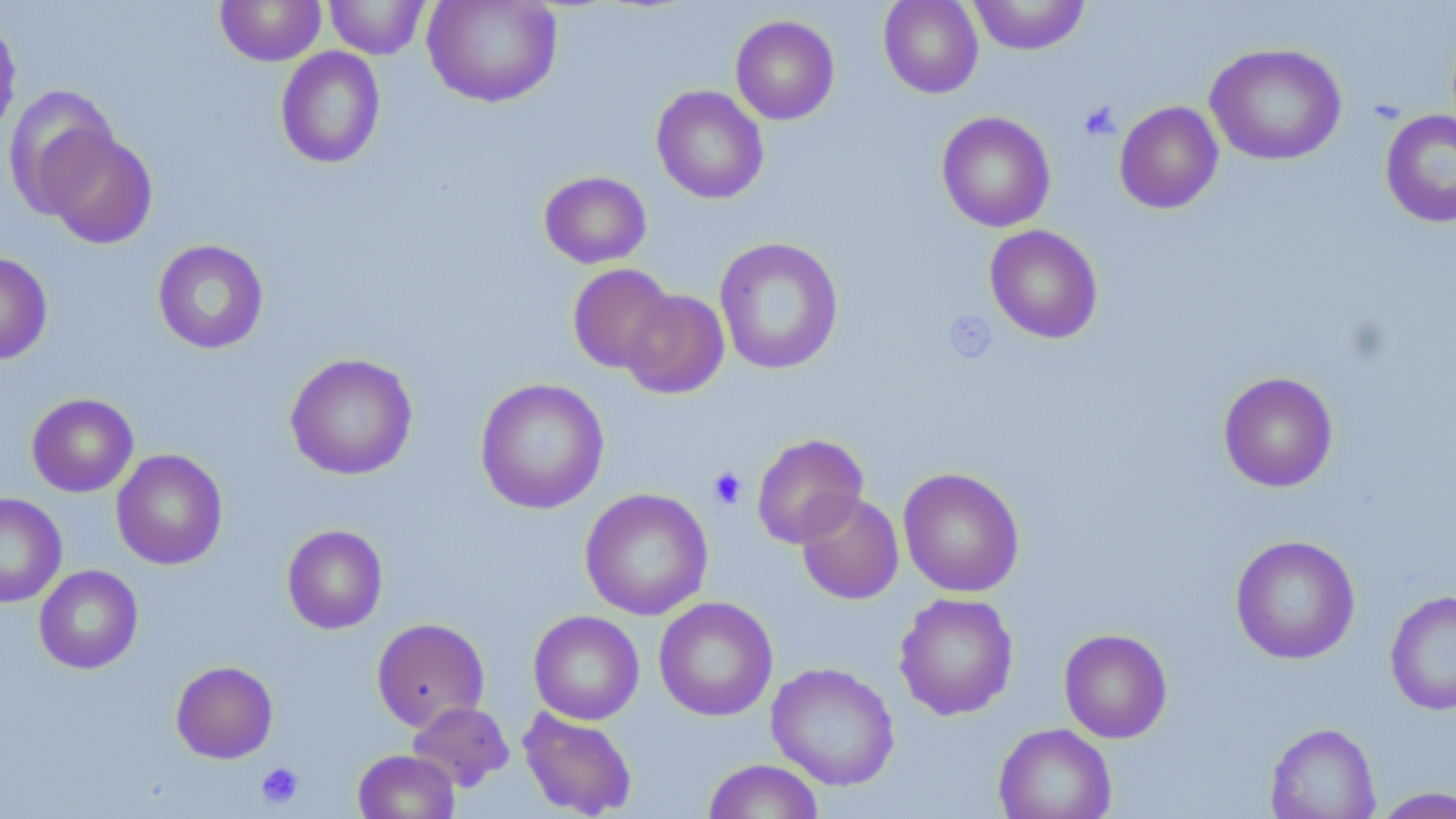
Summary:
  - Coordinate format: approximate bounding boxes as named x1/y1/x2/y2 corners in pixels
  - Uninfected red blood cell locations: (x1=215, y1=0, x2=326, y2=66), (x1=324, y1=0, x2=430, y2=59), (x1=422, y1=0, x2=563, y2=108), (x1=879, y1=0, x2=984, y2=98), (x1=968, y1=0, x2=1090, y2=55), (x1=0, y1=11, x2=22, y2=141), (x1=730, y1=15, x2=840, y2=125), (x1=1205, y1=42, x2=1347, y2=166), (x1=275, y1=46, x2=386, y2=169), (x1=4, y1=84, x2=120, y2=217), (x1=651, y1=85, x2=769, y2=204), (x1=1114, y1=101, x2=1224, y2=214), (x1=1379, y1=109, x2=1456, y2=228), (x1=936, y1=111, x2=1056, y2=233), (x1=43, y1=129, x2=158, y2=249), (x1=538, y1=171, x2=652, y2=269), (x1=984, y1=225, x2=1104, y2=344), (x1=714, y1=237, x2=844, y2=375), (x1=152, y1=239, x2=269, y2=354), (x1=0, y1=252, x2=53, y2=365), (x1=567, y1=263, x2=676, y2=374), (x1=620, y1=289, x2=730, y2=400), (x1=285, y1=353, x2=418, y2=480), (x1=1218, y1=371, x2=1338, y2=492), (x1=475, y1=378, x2=610, y2=514), (x1=26, y1=393, x2=139, y2=497), (x1=751, y1=433, x2=869, y2=548), (x1=111, y1=449, x2=228, y2=570), (x1=898, y1=467, x2=1025, y2=598), (x1=579, y1=487, x2=713, y2=621), (x1=795, y1=491, x2=904, y2=605), (x1=0, y1=493, x2=67, y2=608), (x1=282, y1=524, x2=388, y2=634), (x1=1230, y1=534, x2=1360, y2=664), (x1=33, y1=565, x2=143, y2=674), (x1=1385, y1=589, x2=1456, y2=716), (x1=894, y1=592, x2=1019, y2=720), (x1=654, y1=596, x2=778, y2=722), (x1=528, y1=610, x2=644, y2=725), (x1=371, y1=617, x2=490, y2=732), (x1=1059, y1=628, x2=1172, y2=743), (x1=170, y1=660, x2=278, y2=763), (x1=766, y1=662, x2=900, y2=791), (x1=407, y1=701, x2=514, y2=792), (x1=517, y1=707, x2=638, y2=819), (x1=1265, y1=722, x2=1380, y2=819), (x1=993, y1=723, x2=1117, y2=819), (x1=353, y1=749, x2=459, y2=819), (x1=702, y1=759, x2=825, y2=819), (x1=1370, y1=787, x2=1456, y2=818)
  - Platelet locations: (x1=1079, y1=101, x2=1121, y2=142), (x1=943, y1=310, x2=998, y2=364), (x1=708, y1=466, x2=747, y2=509), (x1=256, y1=762, x2=305, y2=809)
  - Slide-level diagnosis: no evidence of blood parasites
  - Preparation: thin blood smear
  - Modality: light microscopy
  - Image size: 1456×819 pixels
  - Stain: May-Grünwald-Giemsa
  - Field of view: one of a larger specimen
  - Magnification: 1000x